Outline each uninfected red blood cell.
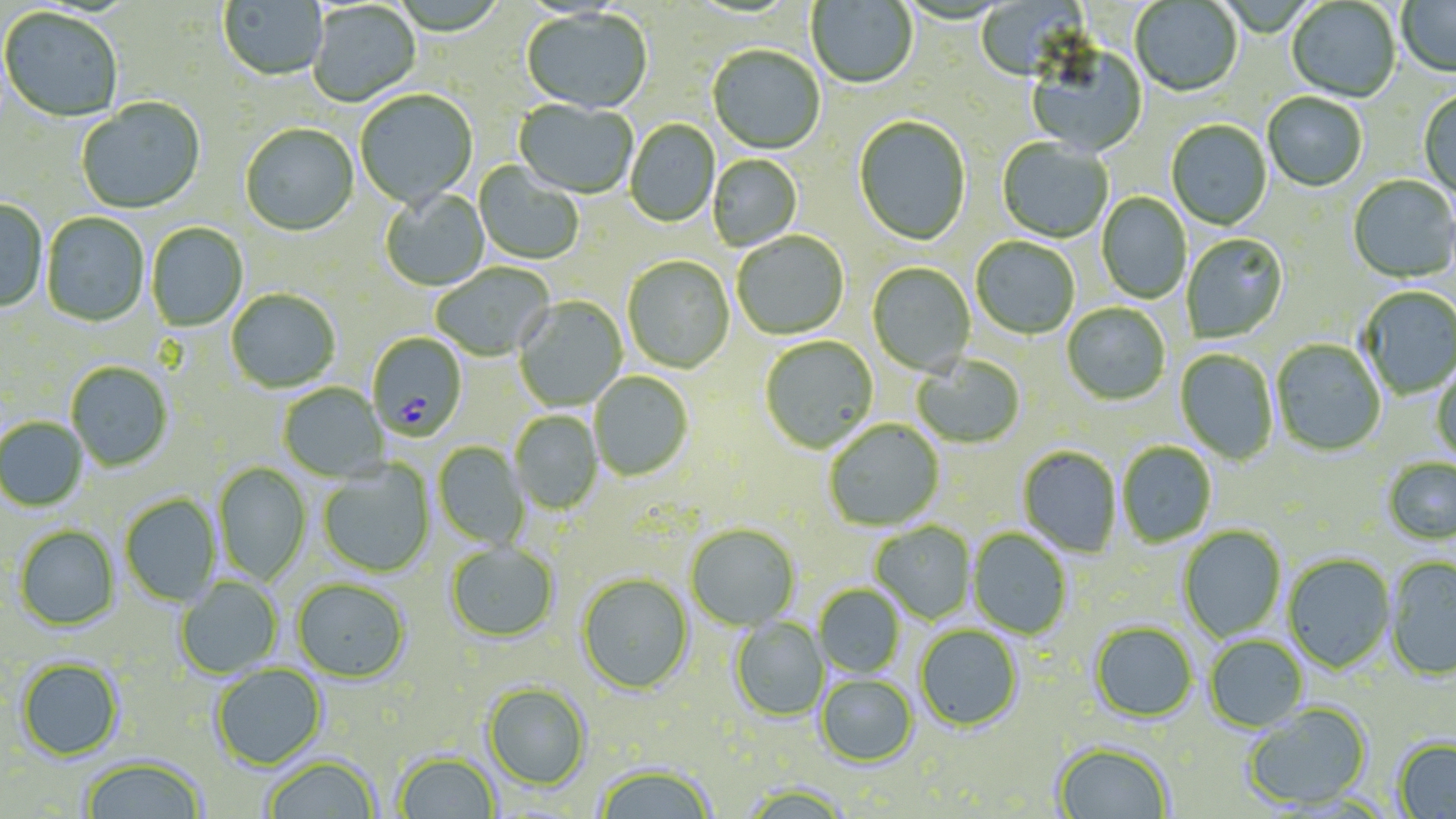

Approximate bounding boxes as (x1,y1)-(x2,y2) corner pairs in pixels.
Uninfected red blood cells: (218,0)-(328,82), (807,0)-(918,90), (975,0)-(1093,83), (1397,0)-(1456,80), (1130,1)-(1242,98), (1287,1)-(1401,103), (308,3)-(421,107), (0,8)-(123,124), (521,10)-(652,115), (707,46)-(825,155), (1026,47)-(1148,157), (354,91)-(478,210), (1419,91)-(1455,199), (1262,93)-(1368,192), (76,98)-(205,215), (513,100)-(638,200), (854,116)-(971,247), (625,119)-(720,228), (1166,121)-(1272,231), (240,125)-(359,237), (997,138)-(1112,243), (708,154)-(803,251), (474,163)-(584,265), (1348,176)-(1456,284), (380,189)-(490,291), (1096,192)-(1191,304), (0,198)-(48,312), (42,212)-(149,327), (146,223)-(248,331), (732,232)-(849,340), (1182,234)-(1289,343), (971,238)-(1080,340), (623,256)-(735,373), (431,262)-(555,361), (867,263)-(976,376), (1358,286)-(1455,399), (226,288)-(340,393), (514,296)-(627,411), (1062,303)-(1170,405), (760,336)-(878,453), (1271,339)-(1386,456), (1175,348)-(1278,465), (912,354)-(1025,448), (66,361)-(173,471), (1431,363)-(1456,464), (589,371)-(693,481), (278,383)-(389,482), (510,411)-(602,514), (0,417)-(88,511), (823,419)-(945,531), (433,442)-(529,549), (1117,442)-(1217,548), (1018,446)-(1122,558), (1382,458)-(1456,544), (213,462)-(311,585), (318,462)-(435,577), (120,494)-(220,606), (870,522)-(977,624), (685,524)-(800,631), (14,525)-(120,631), (1179,526)-(1286,642), (968,528)-(1072,639), (446,542)-(559,642), (1283,553)-(1396,673), (1385,556)-(1456,682), (577,572)-(694,694), (175,577)-(283,678), (292,579)-(410,683), (815,584)-(905,678), (730,617)-(829,721), (1090,621)-(1198,722), (915,625)-(1022,731), (1204,635)-(1309,731), (16,657)-(124,761), (210,664)-(327,770), (816,674)-(917,767), (483,682)-(591,789), (1242,703)-(1371,810), (1393,738)-(1456,818), (1052,741)-(1174,819), (393,751)-(500,818), (81,755)-(207,819), (263,756)-(379,818), (594,764)-(716,819), (741,782)-(854,819).

slide-level diagnosis = Plasmodium falciparum
field of view = single
modality = light microscopy
stain = May-Grünwald-Giemsa
magnification = 1000x
Plasmodium falciparum-infected red blood cell locations = approximate bounding boxes as (x1,y1)-(x2,y2) corner pairs in pixels: (374,332)-(465,443)
preparation = thin blood smear
image size = 1456×819 pixels